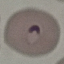

Summary:
  - Result: malaria parasites identified
  - Image type: automatically extracted cell patch, resized to 64 × 64 pixels
  - Capture: smartphone camera at the microscope eyepiece
  - Stain: Giemsa
  - Preparation: thin smear